Evaluate for Plasmodium parasites.
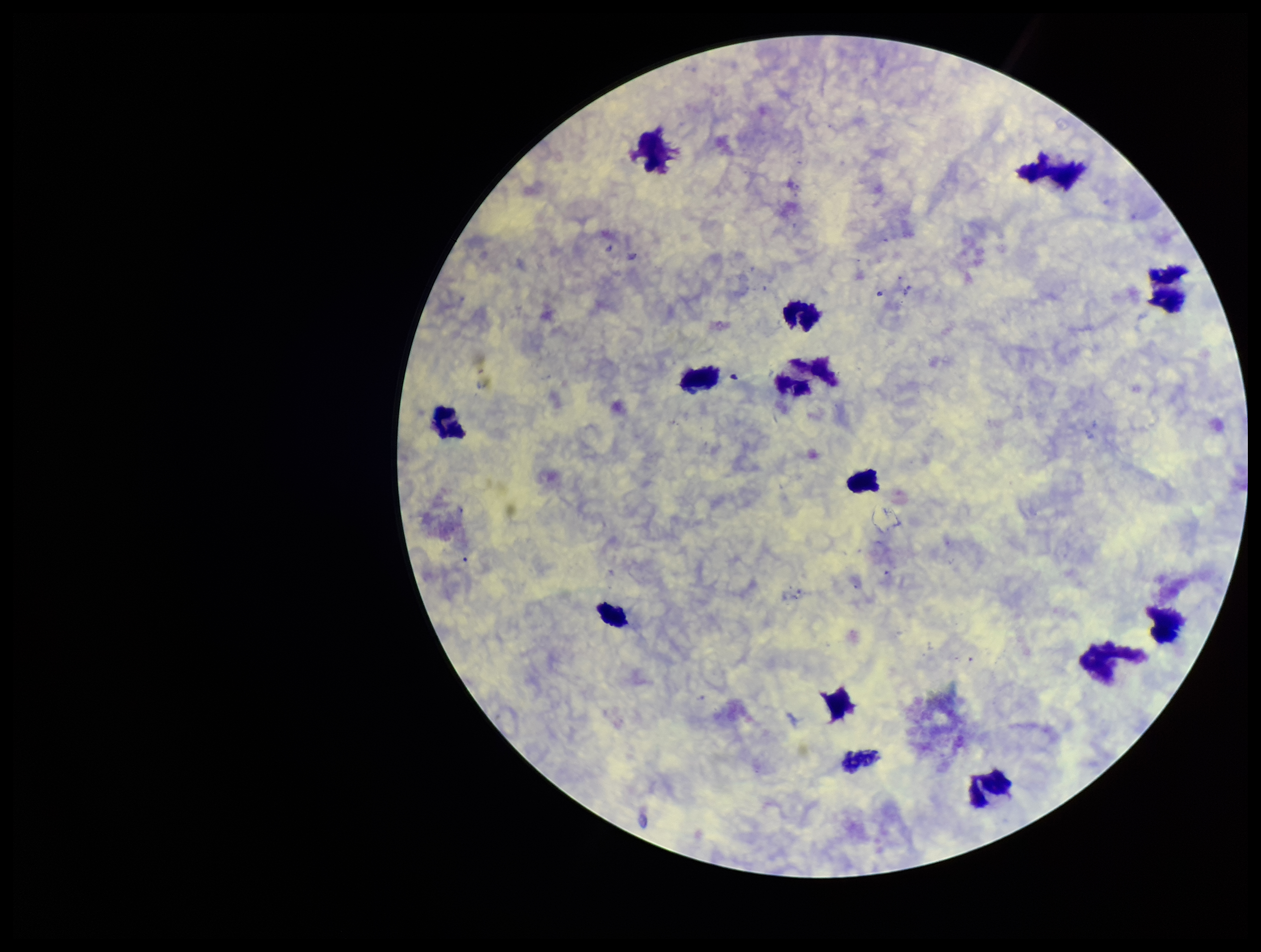

None identified.

capture = smartphone photograph through the microscope eyepiece
image size = 1261×952 pixels
preparation = thick smear
leukocyte count = 14
patient malaria status = negative
parasite count = 0
stain = Giemsa
field of view = single